Assess this cell for malaria.
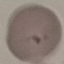

It is parasitized.

Summary:
  - Capture: smartphone through the microscope eyepiece
  - Preparation: thin blood smear
  - Stain: Giemsa
  - Image type: cell patch, automatically extracted from a larger field of view and resized to 64 × 64 pixels